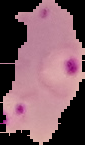
result: malaria parasites detected
preparation: thin blood smear
image_size: 85×145 pixels
image_type: segmented cell region with the area outside set to black